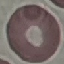
Malaria status: uninfected. Photographed with a smartphone camera at the microscope eyepiece. Thin smear of blood. Cell patch, automatically extracted from a larger field of view and resized to 64 × 64 pixels. Giemsa-stained preparation.